Assess for malaria.
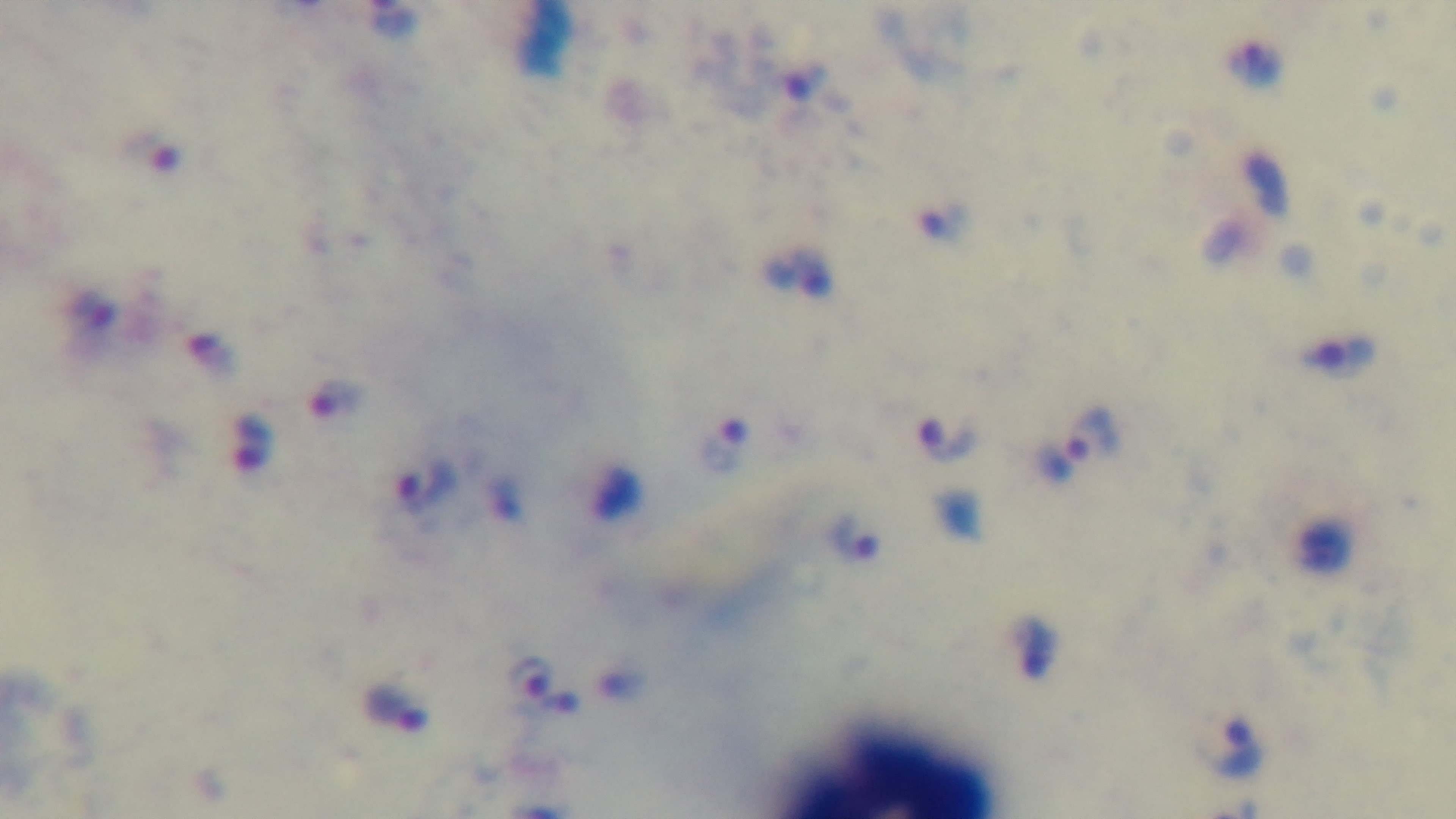
Infected.

{
  "preparation": "thick",
  "objective": "100x oil immersion",
  "field_of_view": "one from the slide",
  "modality": "light microscopy",
  "stain": "Giemsa",
  "capture": "mounted 4K digital camera"
}